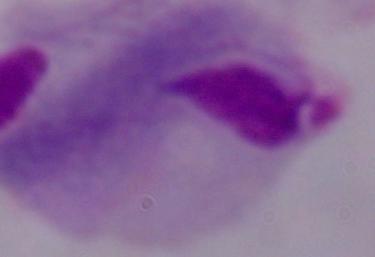

modality = micrograph
magnification = 1000x
identification = trichomonad